Evaluate for Plasmodium parasites.
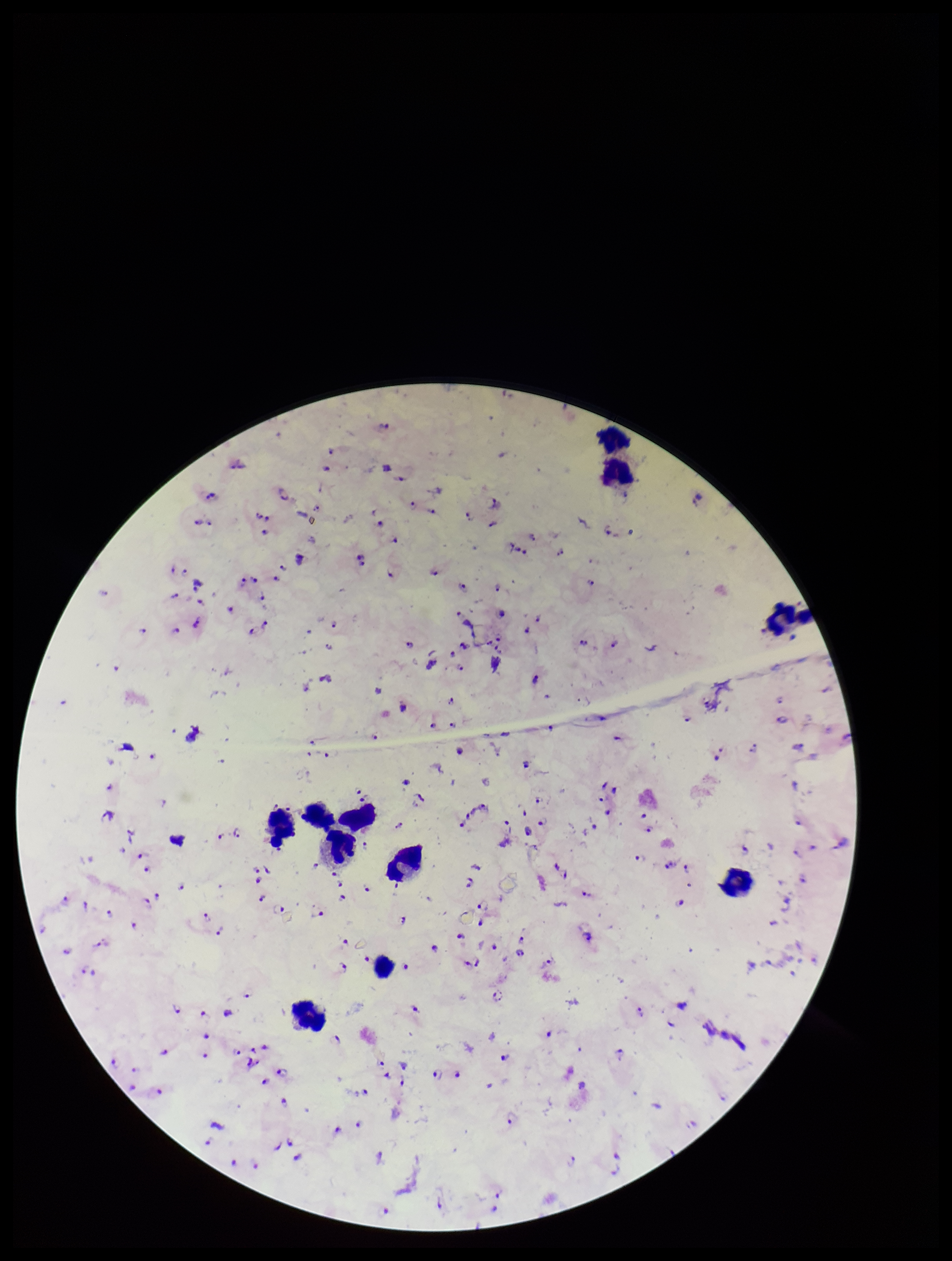

Seen.

patient_malaria_status: infected
leukocyte_count: 11
image_size: 952×1261 pixels
field_of_view: single
species_reported_for_this_patient: Plasmodium falciparum
preparation: thick blood smear
capture: smartphone photograph through the microscope eyepiece
stain: Giemsa
parasite_count: 134